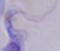
{
  "modality": "photomicrograph",
  "identification": "trypanosome",
  "magnification": "1000x"
}